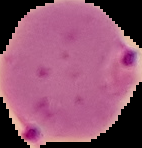
preparation: thin blood smear
malaria_status: parasitized
image_type: segmented cell region with the area outside set to black
image_size: 142×148 pixels